Assess the morphology of the erythrocytes.
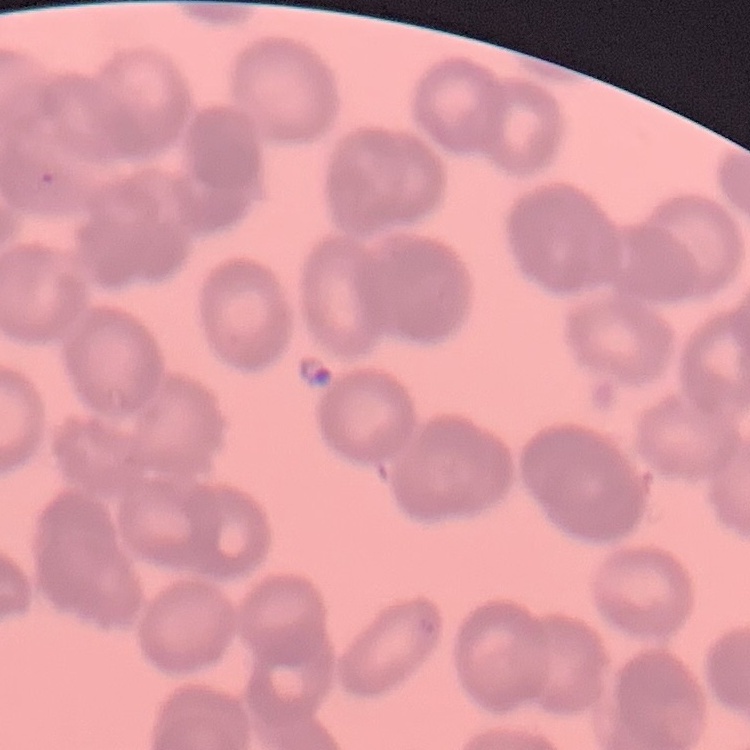
They show rouleaux formation.

preparation = thin blood smear
stain = Field's or Giemsa
image type = one tile cut from a larger photomicrograph